Assess this cell for malaria.
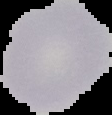
Uninfected.

{
  "image_type": "segmented cell region on a black background",
  "image_size": "112×115 pixels",
  "preparation": "thin blood smear"
}